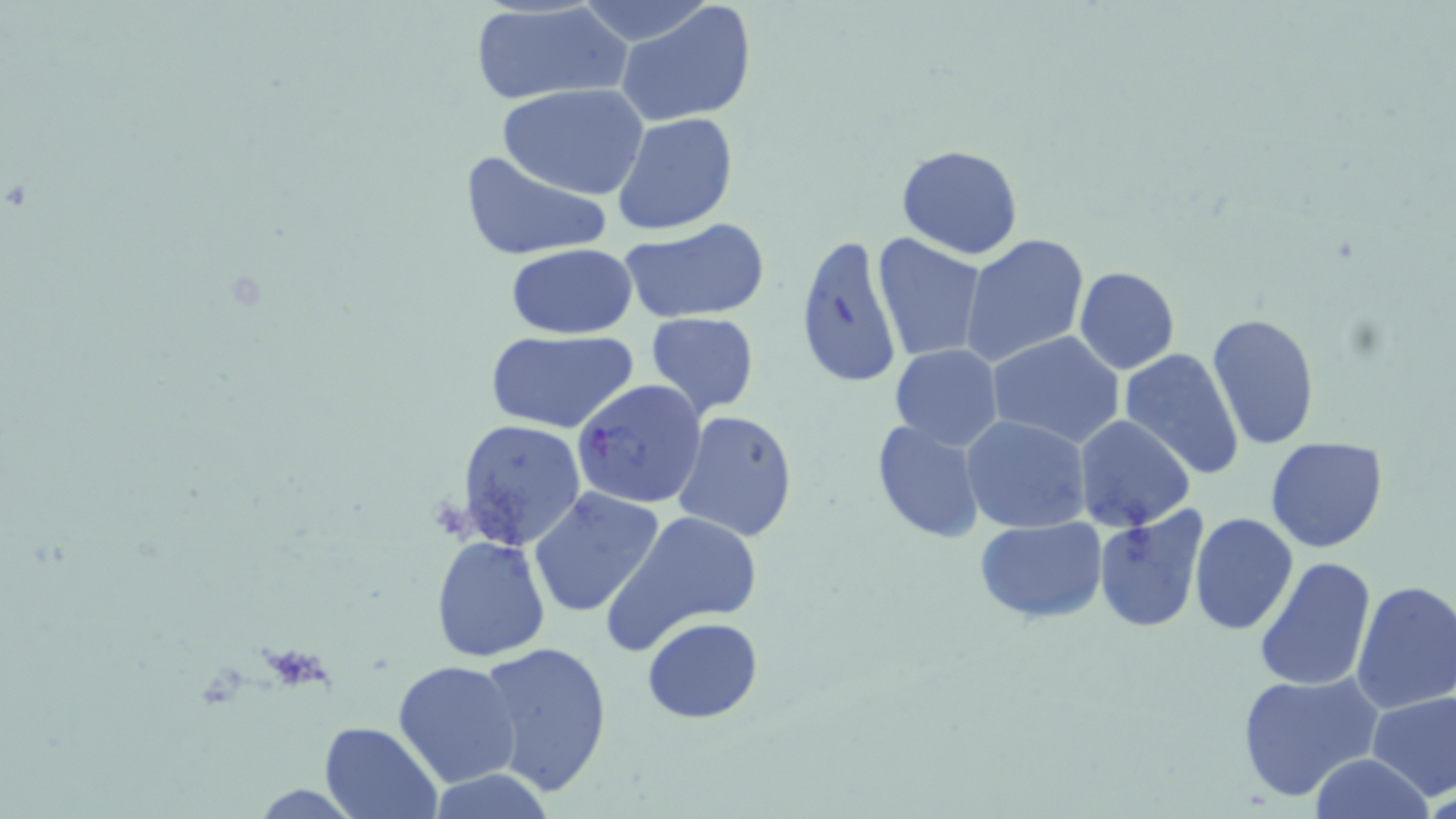

Plasmodium falciparum-infected red blood cell locations = approximate bounding boxes as named x1/y1/x2/y2 corners in pixels: (x1=571, y1=376, x2=708, y2=510)
slide-level diagnosis = Plasmodium falciparum
field of view = one of a larger specimen
modality = optical microscopy
uninfected red blood cell locations = approximate bounding boxes as named x1/y1/x2/y2 corners in pixels: (x1=615, y1=2, x2=758, y2=127), (x1=467, y1=3, x2=631, y2=106), (x1=499, y1=84, x2=649, y2=199), (x1=612, y1=112, x2=739, y2=237), (x1=895, y1=144, x2=1023, y2=260), (x1=459, y1=148, x2=613, y2=261), (x1=617, y1=217, x2=772, y2=324), (x1=794, y1=232, x2=904, y2=390), (x1=961, y1=233, x2=1091, y2=366), (x1=871, y1=234, x2=987, y2=363), (x1=504, y1=243, x2=638, y2=341), (x1=1073, y1=267, x2=1179, y2=374), (x1=643, y1=311, x2=760, y2=417), (x1=1207, y1=313, x2=1320, y2=449), (x1=487, y1=330, x2=639, y2=434), (x1=987, y1=331, x2=1125, y2=449), (x1=888, y1=344, x2=1003, y2=451), (x1=1119, y1=347, x2=1247, y2=479), (x1=672, y1=410, x2=799, y2=542), (x1=1072, y1=415, x2=1193, y2=531), (x1=962, y1=416, x2=1091, y2=533), (x1=869, y1=418, x2=987, y2=543), (x1=455, y1=419, x2=587, y2=548), (x1=1265, y1=436, x2=1389, y2=554), (x1=528, y1=485, x2=666, y2=617), (x1=1092, y1=509, x2=1209, y2=634), (x1=602, y1=511, x2=764, y2=656), (x1=1190, y1=513, x2=1297, y2=635), (x1=975, y1=518, x2=1106, y2=622), (x1=430, y1=535, x2=551, y2=663), (x1=1253, y1=556, x2=1377, y2=692), (x1=1350, y1=579, x2=1456, y2=714), (x1=642, y1=617, x2=764, y2=725), (x1=475, y1=638, x2=615, y2=798), (x1=394, y1=660, x2=524, y2=790), (x1=1238, y1=670, x2=1381, y2=802), (x1=1366, y1=690, x2=1456, y2=800), (x1=319, y1=721, x2=440, y2=818), (x1=1308, y1=753, x2=1434, y2=819), (x1=426, y1=771, x2=560, y2=818), (x1=1426, y1=775, x2=1455, y2=818)
stain = May-Grünwald-Giemsa
preparation = thin blood smear
image size = 1456×819 pixels
magnification = 1000x